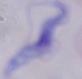
Summary:
  - Modality: micrograph
  - Identification: trypanosome
  - Magnification: 1000x